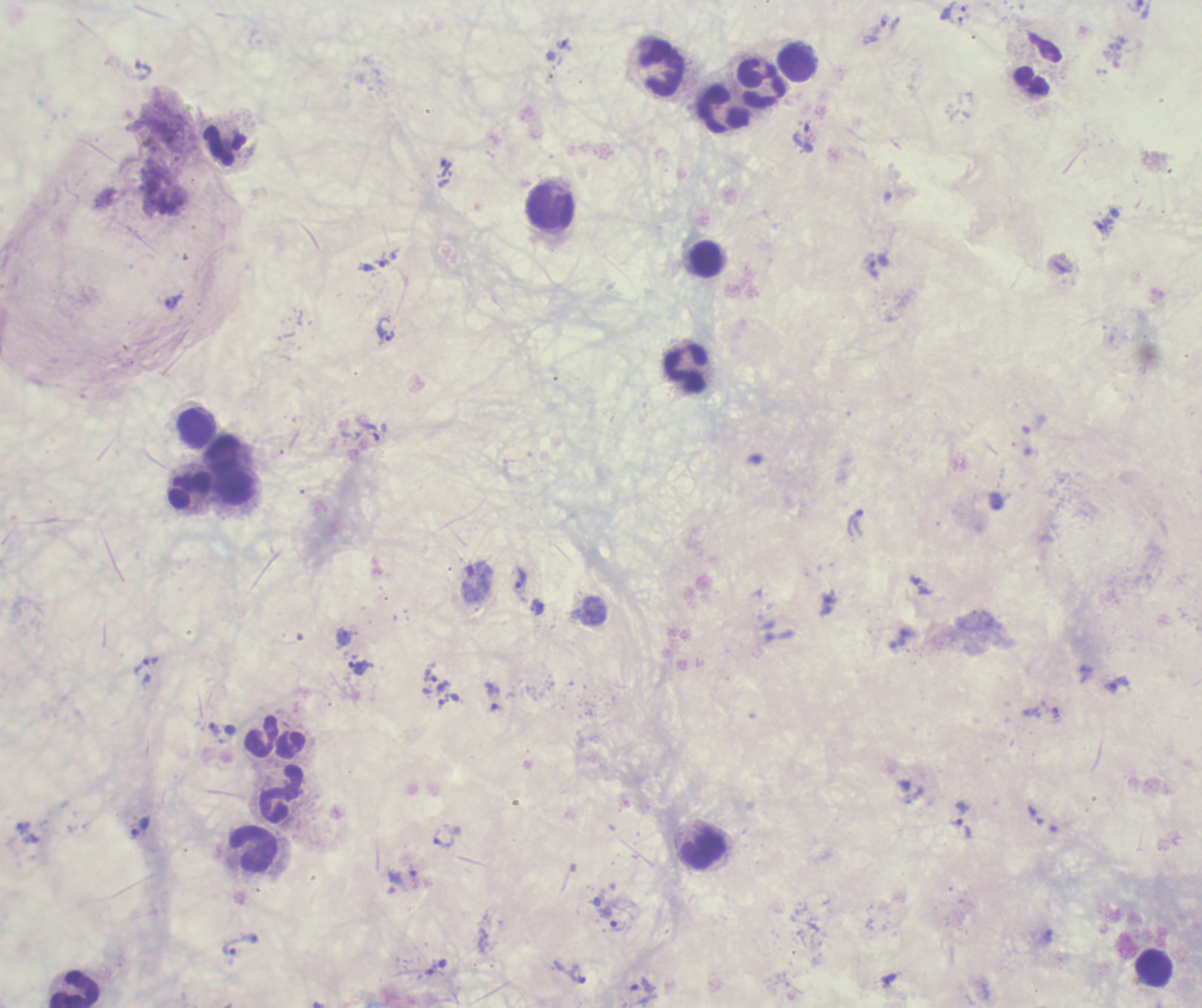 Approximate centers as (x, y) in pixels. Leukocyte locations: (797, 64), (662, 68), (762, 83), (725, 110), (225, 146), (550, 207), (707, 259), (686, 369), (195, 429), (223, 453), (234, 489), (190, 490), (262, 737), (282, 793), (704, 849), (254, 850), (1153, 968), (75, 989). Trophozoite locations: (960, 22), (878, 26), (563, 43), (803, 138), (444, 167), (1103, 227), (382, 259), (872, 266), (173, 302), (386, 329), (367, 433), (856, 522), (521, 578), (538, 608), (344, 636), (147, 665), (358, 668), (431, 675), (1116, 685), (444, 701), (496, 709), (1055, 712), (215, 729), (957, 822), (140, 827), (444, 838), (613, 927), (240, 944), (578, 973), (889, 979), (642, 985). Background quality: unsatisfactory. Thick smear of blood. Previously used in a real diagnosis. 100x magnification. Single field of view. Image is 1202×1008 pixels. Coloration quality: bad. Result: malaria parasites identified. Romanowsky-stained preparation.